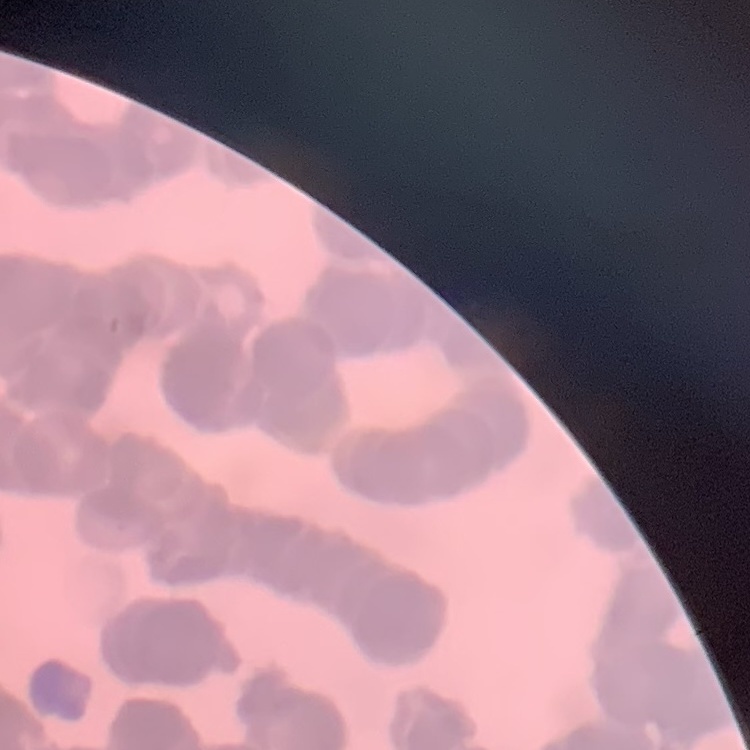

Summary:
  - Red blood cell morphology: rouleaux formation
  - Stain: Field's or Giemsa
  - Preparation: thin peripheral smear
  - Image type: square crop of a larger photomicrograph